Identify the blood parasite species.
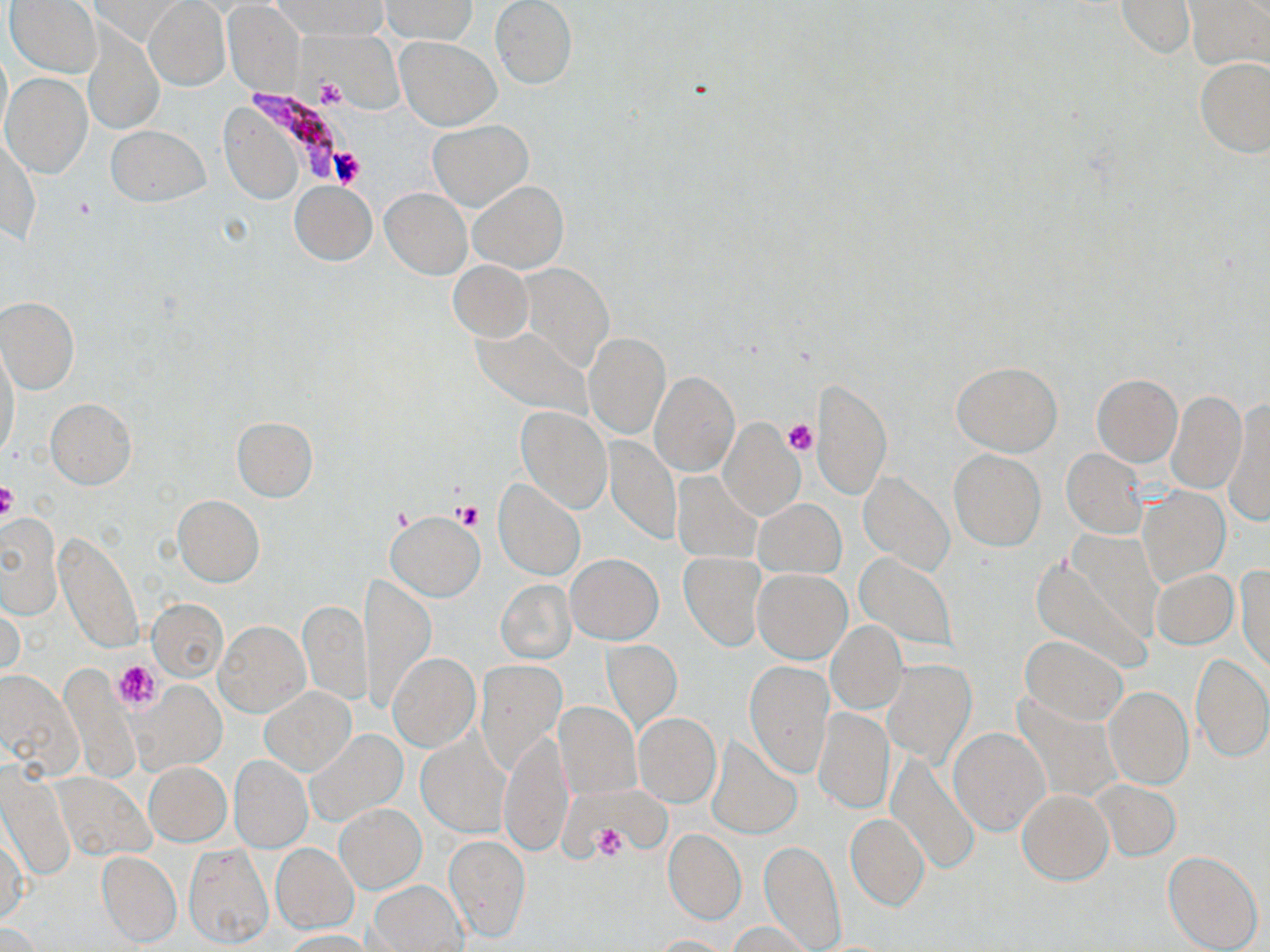
Plasmodium falciparum.

field of view = one of a larger specimen
magnification = 1000x
uninfected red blood cell locations = approximate bounding boxes as (x1,y1)-(x2,y2) corner pairs in pixels: (6,0)-(102,77), (381,0)-(477,43), (1182,0)-(1269,73), (275,1)-(386,40), (490,1)-(576,90), (144,2)-(230,91), (1116,2)-(1195,60), (222,3)-(304,96), (82,26)-(164,135), (395,35)-(501,130), (0,44)-(11,146), (1195,56)-(1270,158), (2,74)-(92,178), (220,108)-(304,205), (427,119)-(534,211), (105,124)-(210,207), (2,135)-(39,243), (289,181)-(376,264), (469,181)-(568,273), (380,188)-(470,279), (448,261)-(532,342), (515,264)-(614,371), (0,297)-(80,395), (471,325)-(592,417), (584,333)-(669,439), (1,345)-(20,464), (951,362)-(1063,455), (650,371)-(740,476), (1092,374)-(1182,466), (809,376)-(891,502), (1167,390)-(1247,493), (44,398)-(137,489), (1221,400)-(1270,525), (515,405)-(612,512), (230,416)-(318,502), (720,422)-(803,520), (604,435)-(681,544), (947,449)-(1045,550), (1061,449)-(1149,538), (856,470)-(953,575), (670,471)-(762,563), (493,479)-(585,580), (1140,486)-(1229,586), (172,496)-(265,587), (754,499)-(845,578), (384,510)-(485,601), (0,512)-(61,619), (56,531)-(143,654), (1030,550)-(1153,674), (678,553)-(766,651), (853,553)-(959,653), (565,554)-(662,643), (1236,563)-(1269,674), (1151,567)-(1237,648), (753,568)-(851,663), (362,573)-(433,711), (497,580)-(576,663), (147,597)-(227,682), (298,599)-(371,706), (1,600)-(22,683), (213,621)-(310,717), (827,622)-(907,713), (1020,635)-(1127,725), (603,639)-(683,734), (388,653)-(480,751), (1191,653)-(1269,762), (882,658)-(974,767), (475,659)-(566,772), (744,660)-(834,777), (60,666)-(140,784), (0,672)-(81,775), (128,679)-(227,775), (1104,685)-(1193,789), (259,687)-(356,775), (555,702)-(640,798), (814,709)-(893,813), (634,713)-(720,806), (948,726)-(1049,836), (304,729)-(407,829), (498,730)-(573,857), (418,735)-(511,837), (707,736)-(801,839), (887,751)-(980,875), (229,755)-(312,854), (145,762)-(231,846), (1,770)-(75,882), (51,771)-(155,864), (1092,782)-(1181,860), (1018,788)-(1112,884), (335,803)-(427,893), (846,814)-(929,910), (664,830)-(745,924), (1,834)-(27,923), (445,834)-(530,942), (759,842)-(845,952), (183,844)-(274,948), (272,844)-(358,933), (96,850)-(182,948), (1164,850)-(1263,952), (368,881)-(466,951), (727,922)-(816,952), (0,923)-(44,952), (281,929)-(373,951), (650,935)-(734,952)
image size = 1270×952 pixels
Plasmodium falciparum-infected red blood cell locations = approximate bounding boxes as (x1,y1)-(x2,y2) corner pairs in pixels: (249,88)-(343,182)
preparation = thin blood film
stain = May-Grünwald-Giemsa
modality = optical microscopy
platelet locations = approximate bounding boxes as (x1,y1)-(x2,y2) corner pairs in pixels: (317,77)-(346,106), (330,149)-(364,188), (71,196)-(95,221), (782,420)-(816,456), (0,482)-(19,523), (455,503)-(485,530), (113,660)-(161,712), (593,824)-(628,860)